State which parasite is depicted.
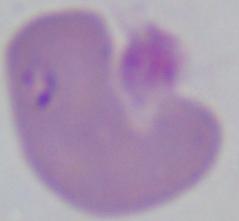

This is Babesia.

Captured at 1000x magnification. Photomicrograph.